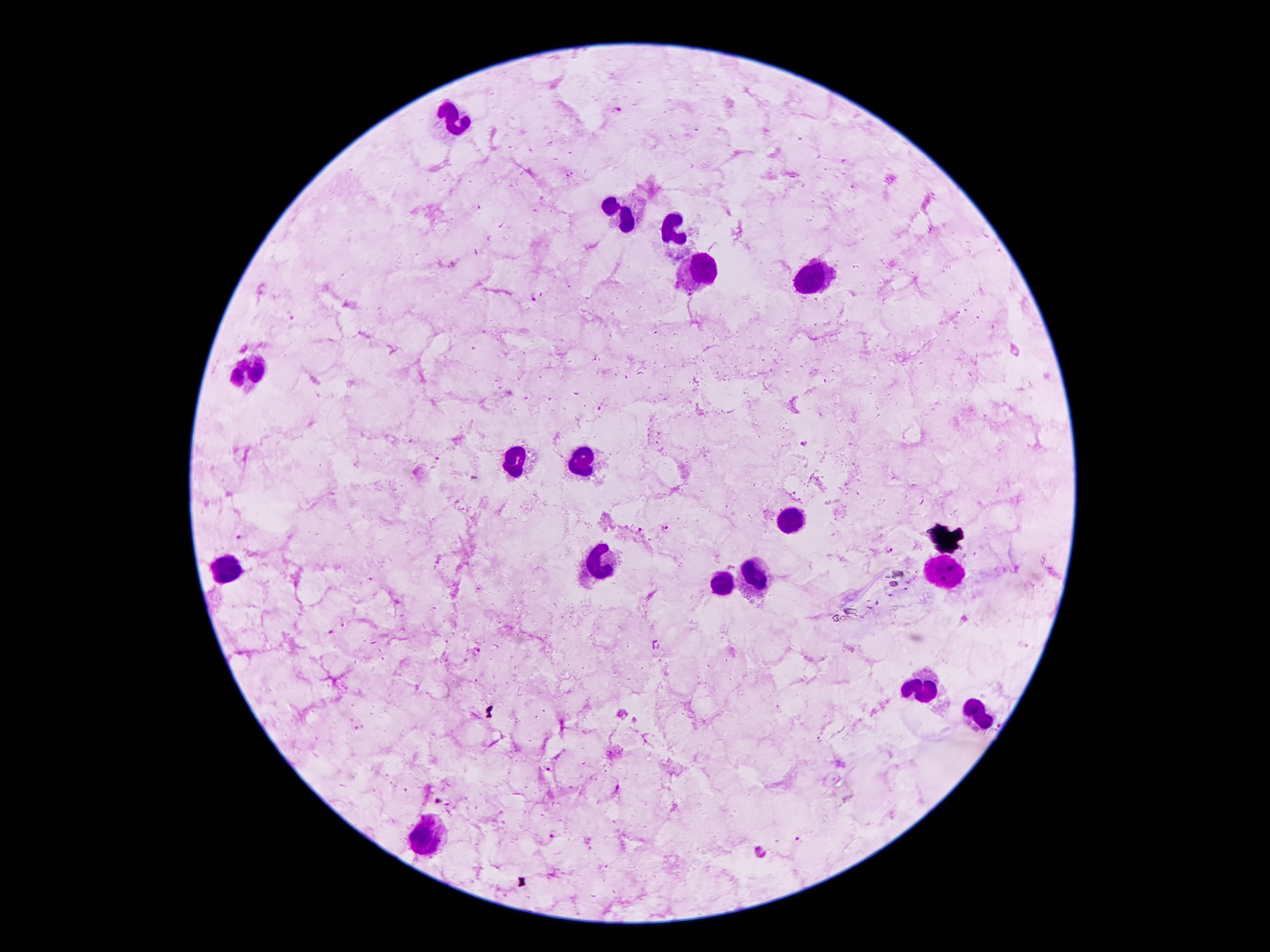
coordinate format = approximate centers as [x, y] in pixels
leukocyte locations = [454, 117], [628, 219], [676, 230], [705, 271], [819, 276], [253, 366], [581, 457], [517, 458], [790, 517], [603, 564], [231, 571], [942, 576], [760, 578], [719, 582], [921, 692], [978, 714], [431, 837]
Plasmodium parasite locations = [616, 111], [534, 298], [805, 443], [667, 528], [240, 535], [889, 550], [963, 618], [331, 633], [477, 650], [441, 802], [553, 834], [798, 840], [761, 852]
magnification = 100x
capture = smartphone camera through the microscope eyepiece
patient malaria status = infected with Plasmodium falciparum
field of view = single
stain = Giemsa
image size = 1270×952 pixels
preparation = thick peripheral-blood smear